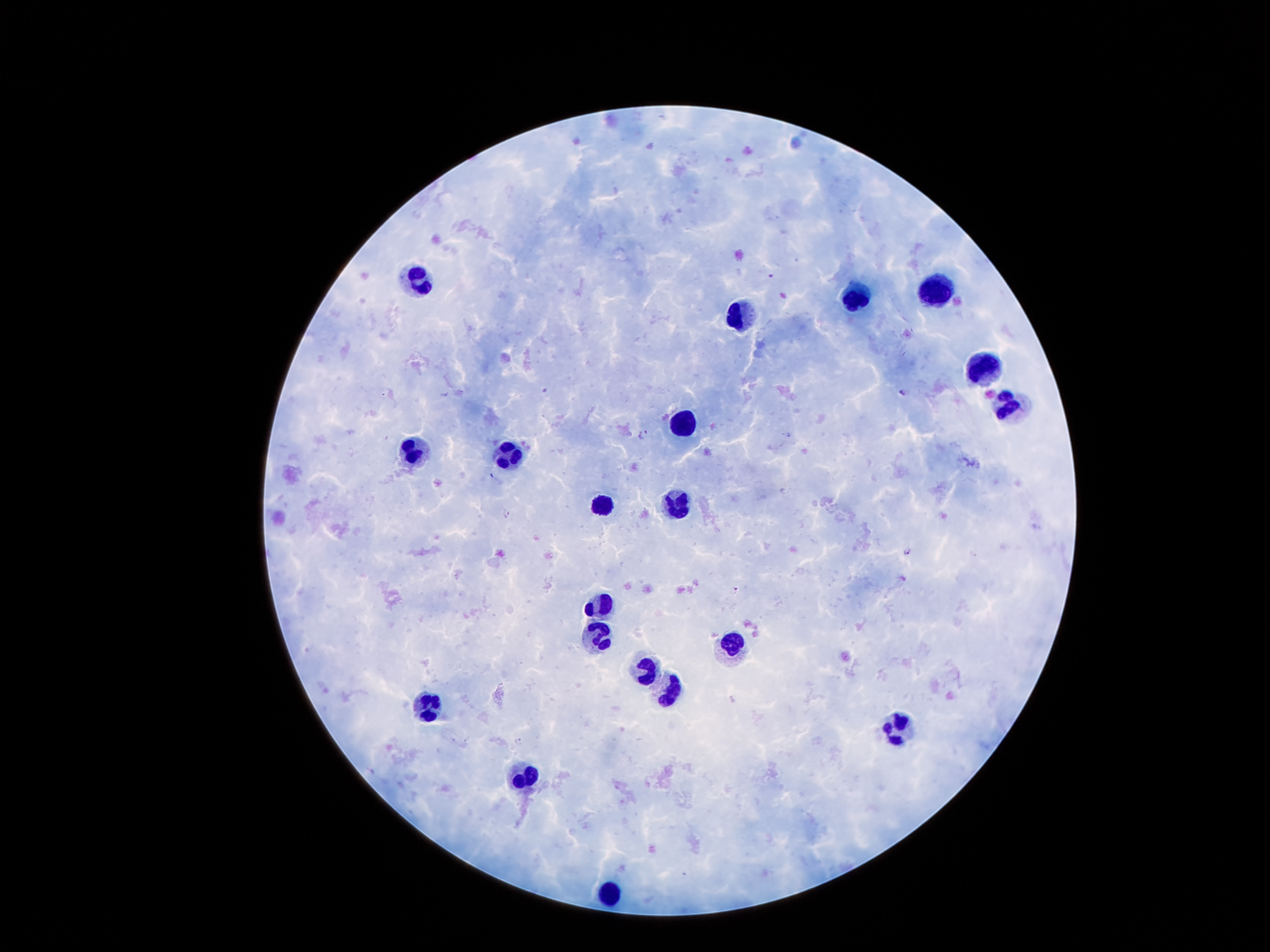

Approximate centers as [x, y] in pixels.
Summary:
  - Leukocyte locations: [417, 279], [936, 290], [859, 296], [743, 313], [974, 368], [1010, 406], [684, 420], [412, 449], [511, 454], [676, 504], [602, 505], [597, 603], [597, 637], [732, 641], [648, 668], [669, 688], [430, 707], [898, 727], [524, 775], [607, 888]
  - Malaria parasite locations: [771, 276], [545, 390], [903, 391], [644, 434], [507, 511], [908, 551], [735, 589], [520, 740]
  - Stain: Giemsa
  - Field of view: one from this slide
  - Capture: smartphone camera through the microscope eyepiece
  - Image size: 1270×952 pixels
  - Magnification: 100x
  - Patient malaria status: positive for Plasmodium falciparum
  - Preparation: thick peripheral-blood smear